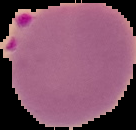
From a thin blood film. Segmented cell region on a black background. Malaria status: parasitized. Image is 136×130 pixels.